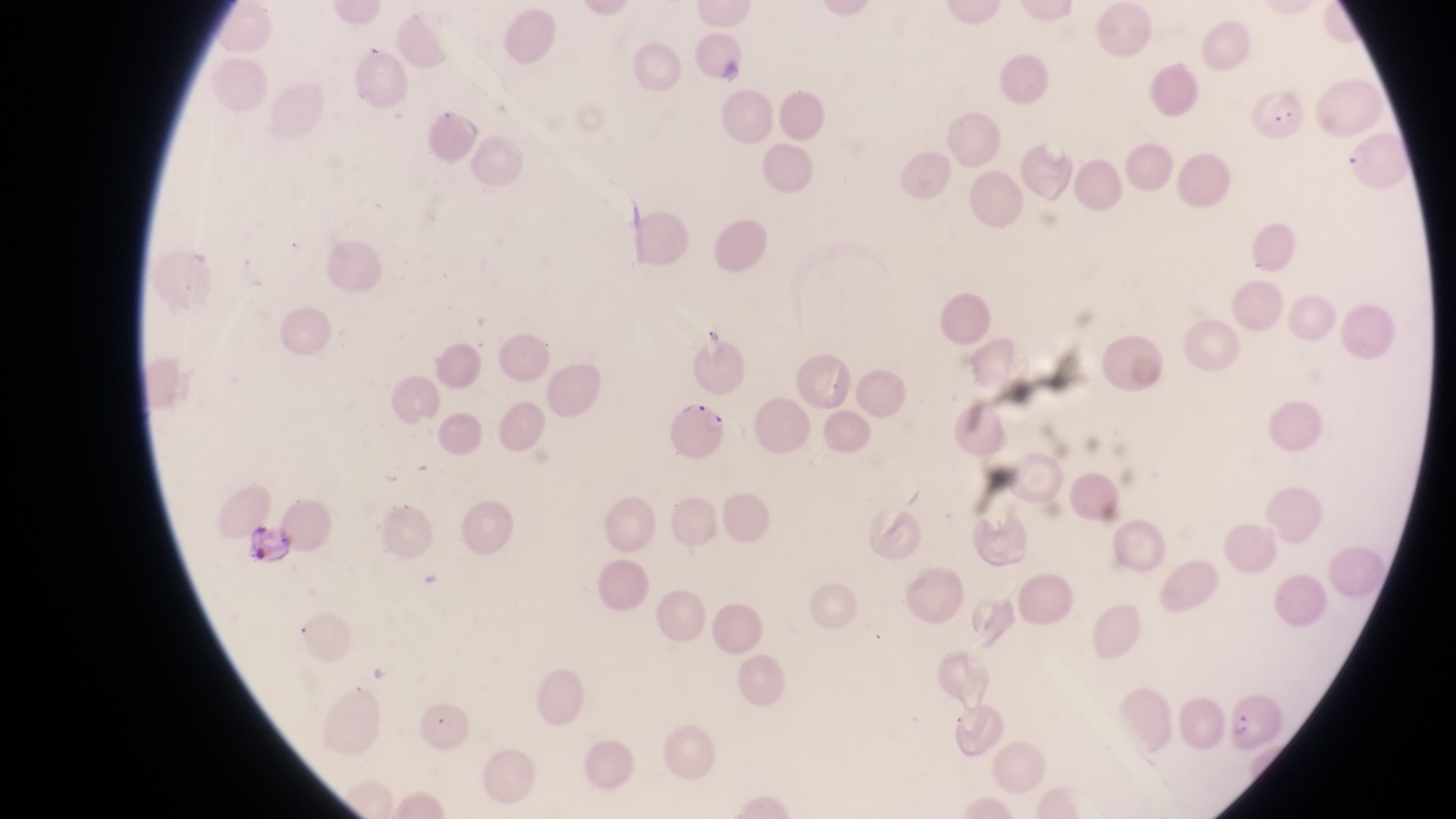
{
  "capture": "smartphone photograph through the eyepiece of an Olympus CX-23 microscope",
  "image_size": "1456×819 pixels",
  "parasitised_red_blood_cell_locations": "approximate bounding boxes as left top right bottom in pixels: 667 399 733 460",
  "country": "Uganda",
  "magnification": "1000x",
  "leukocyte_locations": "approximate bounding boxes as left top right bottom in pixels: 246 519 294 567",
  "preparation": "thin blood smear",
  "field_of_view": "single"
}